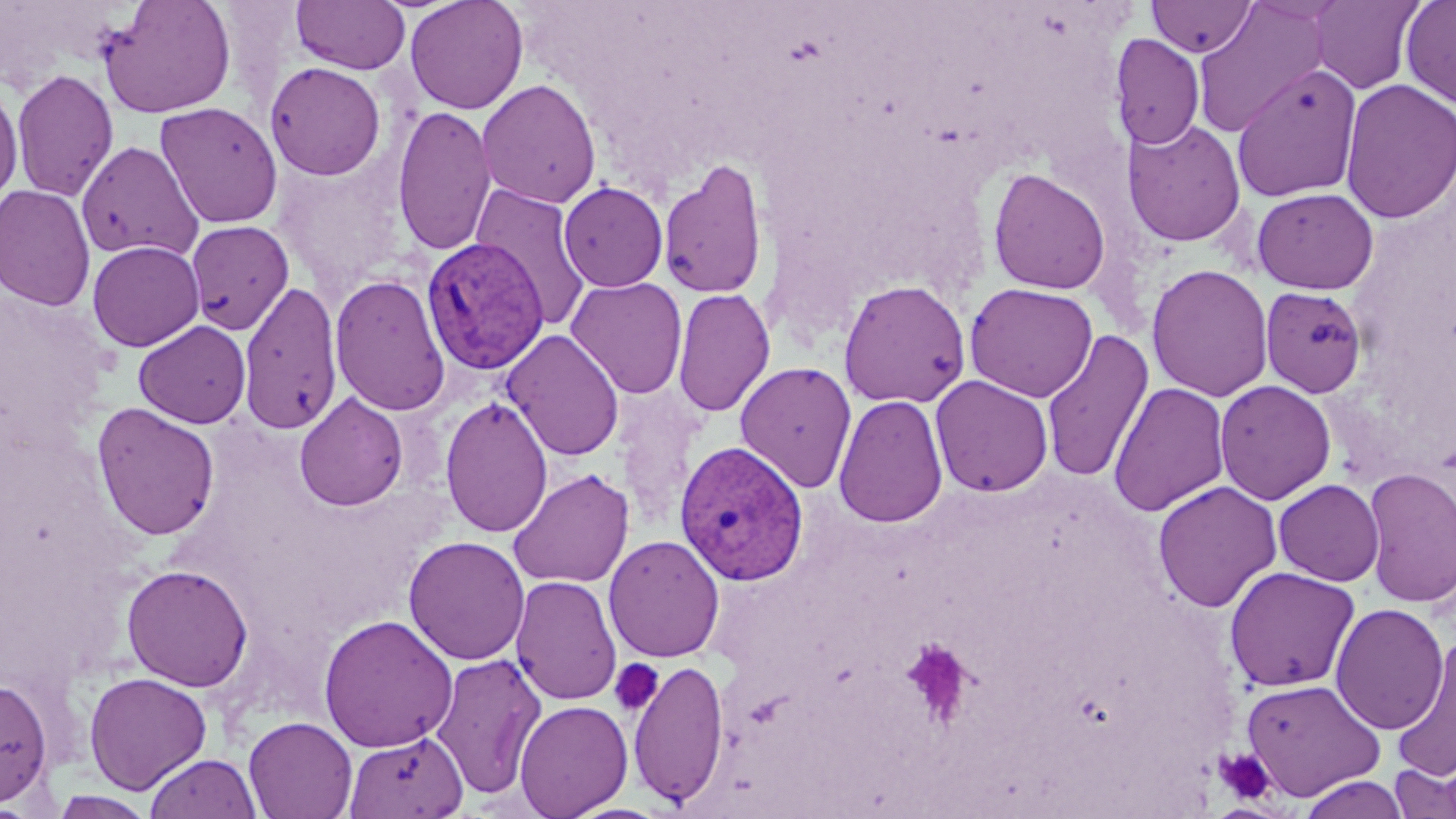
Summary:
  - Coordinate format: approximate bounding boxes as [x1, y1, x2, y2] in pixels
  - Uninfected red blood cell locations: [98, 0, 237, 119], [291, 0, 410, 75], [404, 0, 529, 115], [1146, 0, 1257, 57], [1191, 0, 1332, 137], [1308, 0, 1426, 94], [1400, 0, 1456, 108], [1109, 33, 1205, 150], [264, 61, 387, 180], [1231, 63, 1363, 204], [11, 68, 119, 202], [477, 78, 602, 209], [1340, 78, 1455, 223], [0, 79, 23, 207], [155, 101, 283, 229], [392, 103, 497, 257], [1121, 118, 1246, 247], [76, 140, 203, 262], [657, 157, 769, 301], [988, 167, 1111, 295], [469, 182, 592, 331], [558, 182, 668, 292], [0, 184, 95, 311], [1251, 187, 1379, 293], [185, 219, 294, 335], [87, 240, 205, 352], [1147, 264, 1273, 402], [330, 274, 451, 416], [566, 276, 688, 398], [837, 278, 972, 408], [238, 281, 343, 435], [964, 282, 1098, 402], [1260, 286, 1368, 398], [672, 287, 775, 418], [134, 320, 251, 428], [502, 329, 624, 461], [1040, 329, 1155, 484], [735, 361, 857, 493], [930, 374, 1054, 497], [1214, 379, 1337, 505], [1108, 381, 1230, 517], [616, 385, 705, 535], [294, 392, 408, 511], [832, 393, 948, 528], [440, 395, 553, 538], [91, 402, 220, 540], [1361, 466, 1456, 608], [507, 468, 634, 589], [1273, 479, 1385, 586], [1152, 480, 1282, 613], [604, 534, 725, 663], [403, 535, 530, 665], [121, 563, 253, 692], [1224, 565, 1361, 693], [510, 575, 622, 705], [1330, 602, 1449, 735], [318, 613, 458, 752], [1391, 635, 1455, 782], [430, 652, 547, 799], [628, 658, 731, 808], [83, 671, 212, 794], [0, 676, 53, 807], [1241, 678, 1386, 801], [514, 699, 632, 818], [243, 715, 357, 819], [344, 730, 468, 818], [144, 753, 260, 819], [1389, 760, 1456, 819], [1298, 774, 1409, 819], [50, 790, 156, 819]
  - Plasmodium vivax-infected red blood cell locations: [421, 236, 549, 375], [674, 440, 809, 586]
  - Platelet locations: [900, 639, 976, 728], [609, 659, 664, 716], [1213, 747, 1276, 804]
  - Slide-level diagnosis: Plasmodium vivax
  - Image size: 1456×819 pixels
  - Field of view: one of a larger specimen
  - Magnification: 1000x
  - Modality: optical microscopy
  - Preparation: thin blood film
  - Stain: May-Grünwald-Giemsa